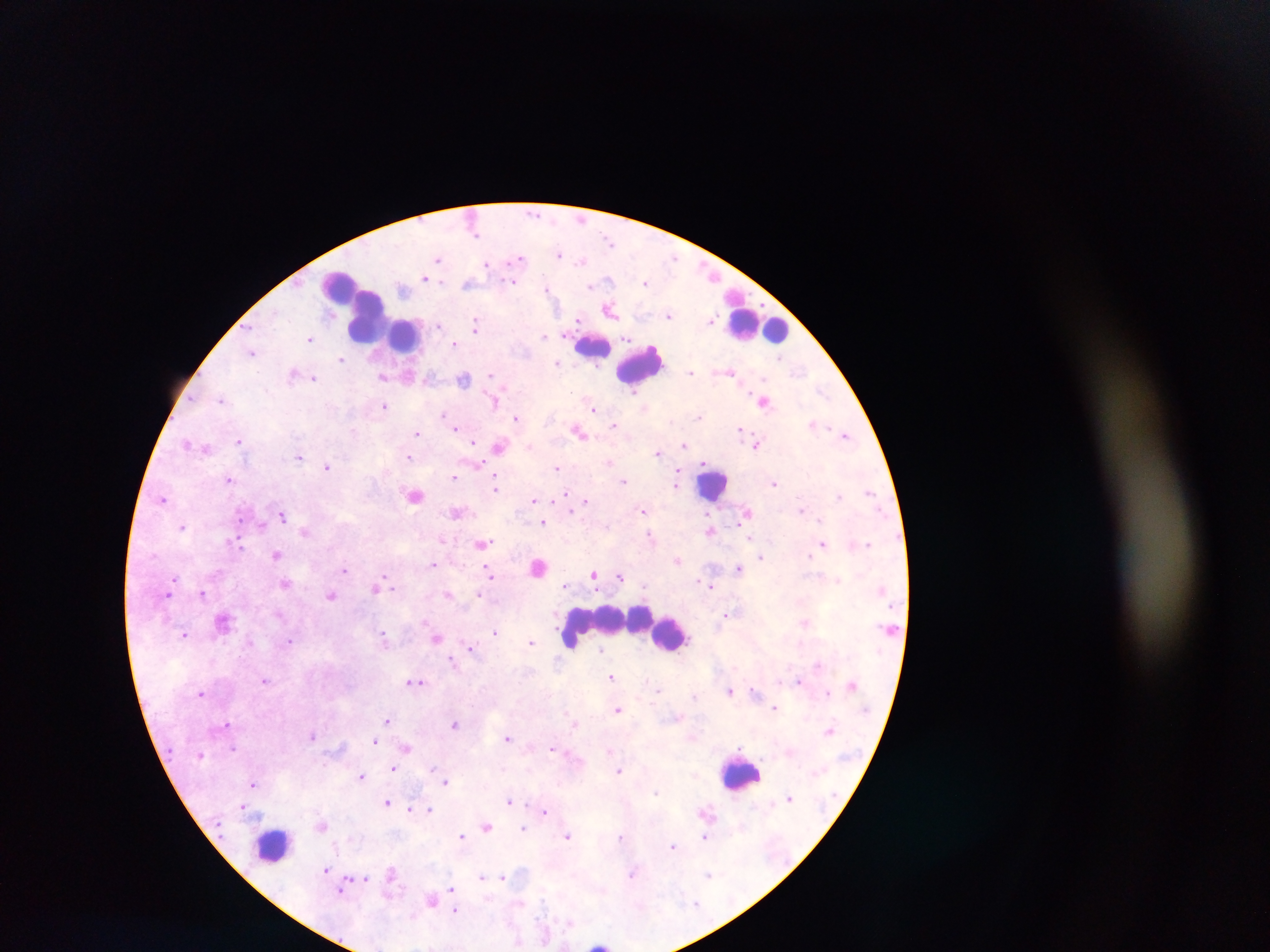
Approximate centers as {x, y} in pixels. Leukocyte locations: {340, 291}, {370, 319}, {759, 325}, {404, 334}, {593, 347}, {641, 363}, {714, 484}, {610, 621}, {672, 633}, {742, 774}, {272, 846}, {601, 942}. Plasmodium parasite locations: {535, 214}, {580, 219}, {476, 232}, {609, 240}, {559, 254}, {673, 257}, {437, 259}, {521, 259}, {583, 260}, {487, 264}, {426, 278}, {609, 279}, {513, 283}, {645, 283}, {467, 284}, {590, 286}, {546, 288}, {403, 289}, {610, 310}, {668, 315}, {578, 319}, {711, 320}, {438, 325}, {476, 325}, {543, 336}, {310, 338}, {628, 338}, {454, 343}, {251, 352}, {780, 357}, {341, 359}, {557, 363}, {690, 372}, {731, 372}, {798, 372}, {294, 374}, {491, 375}, {409, 376}, {383, 377}, {314, 378}, {764, 378}, {464, 379}, {821, 391}, {634, 393}, {221, 399}, {494, 401}, {763, 401}, {384, 406}, {594, 408}, {444, 414}, {699, 417}, {517, 418}, {813, 423}, {614, 425}, {455, 428}, {740, 429}, {417, 432}, {579, 432}, {844, 434}, {239, 441}, {473, 442}, {187, 443}, {529, 445}, {684, 445}, {756, 445}, {499, 446}, {206, 448}, {658, 452}, {300, 457}, {409, 457}, {609, 462}, {704, 463}, {479, 464}, {327, 466}, {557, 468}, {677, 475}, {453, 477}, {229, 479}, {496, 479}, {624, 482}, {774, 483}, {676, 485}, {496, 486}, {869, 492}, {414, 495}, {840, 495}, {567, 496}, {163, 499}, {534, 500}, {585, 502}, {537, 505}, {570, 508}, {801, 509}, {643, 510}, {457, 512}, {747, 513}, {283, 516}, {819, 520}, {543, 522}, {262, 525}, {182, 526}, {709, 529}, {304, 532}, {649, 535}, {751, 538}, {443, 541}, {234, 542}, {754, 542}, {482, 544}, {823, 544}, {868, 544}, {276, 554}, {810, 556}, {761, 557}, {678, 561}, {433, 564}, {742, 565}, {538, 568}, {739, 568}, {344, 570}, {594, 573}, {490, 574}, {620, 576}, {174, 579}, {838, 580}, {285, 584}, {565, 584}, {644, 586}, {711, 586}, {375, 588}, {168, 591}, {203, 594}, {448, 594}, {479, 594}, {331, 595}, {728, 614}, {224, 622}, {805, 623}, {494, 632}, {184, 635}, {383, 635}, {438, 638}, {289, 641}, {531, 642}, {471, 647}, {600, 650}, {452, 659}, {818, 665}, {611, 677}, {265, 681}, {799, 681}, {416, 682}, {851, 685}, {658, 689}, {730, 691}, {201, 692}, {754, 692}, {826, 693}, {694, 696}, {775, 707}, {617, 710}, {387, 720}, {226, 724}, {455, 724}, {574, 724}, {830, 730}, {313, 734}, {507, 738}, {375, 740}, {233, 748}, {406, 748}, {553, 748}, {610, 751}, {395, 768}, {433, 768}, {619, 771}, {361, 776}, {446, 782}, {253, 784}, {657, 792}, {790, 798}, {509, 800}, {386, 803}, {244, 806}, {410, 809}, {430, 809}, {545, 811}, {322, 826}, {486, 826}, {523, 828}, {461, 836}, {568, 836}, {620, 837}, {705, 838}, {672, 846}, {326, 869}, {391, 872}, {632, 874}, {708, 874}, {482, 877}, {503, 877}, {365, 879}, {342, 889}, {451, 889}, {431, 900}, {455, 910}. Thick blood smear. Sample from Ghana. Photographed through a microscope with a mobile-phone camera. Image is 1270×952 pixels. Single field of view.